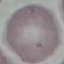 Result: no malaria parasites detected. Automatically extracted cell patch, resized to 64 × 64 pixels. Photographed with a smartphone camera at the microscope eyepiece. Thin blood film. Giemsa-stained preparation.